Report the malaria status of this cell.
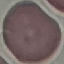

Uninfected.

Summary:
  - Preparation: thin blood film
  - Capture: smartphone through the microscope eyepiece
  - Image type: cell patch, automatically extracted from a larger field of view and resized to 64 × 64 pixels
  - Stain: Giemsa